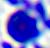
Summary:
  - Identification: leukocyte
  - Modality: micrograph
  - Magnification: 400x